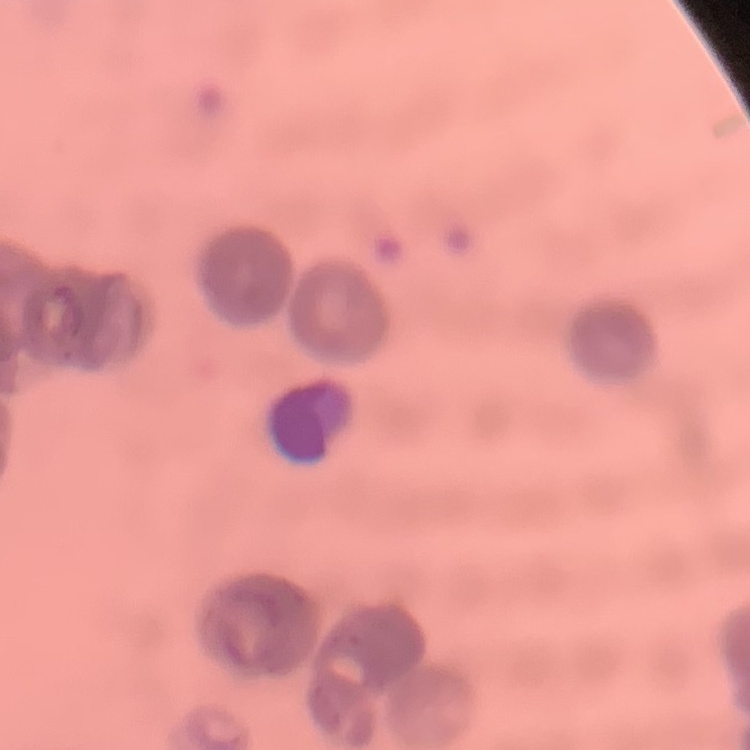
erythrocyte morphology = rouleaux formation
stain = Field's or Giemsa
preparation = thin blood film
image type = one tile cut from a larger photomicrograph